Comment on the morphology of the erythrocytes.
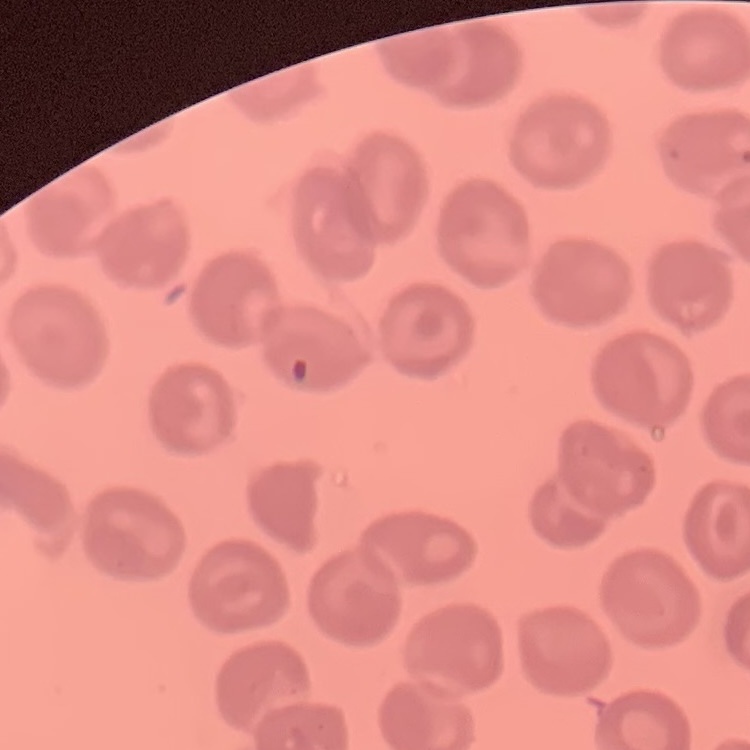
No rouleaux formation.

Summary:
  - Stain: Field's or Giemsa
  - Image type: square crop of a larger photomicrograph
  - Preparation: thin peripheral smear